Name the parasite shown.
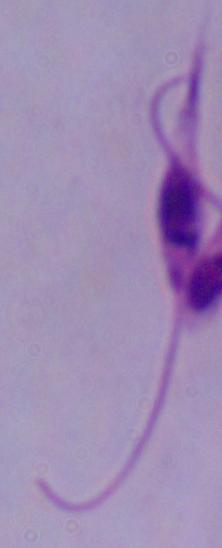
Leishmania.

Captured at 1000x magnification. Micrograph.